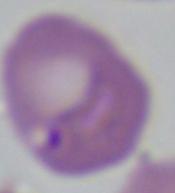

Summary:
  - Magnification: 1000x
  - Modality: photomicrograph
  - Identification: Babesia